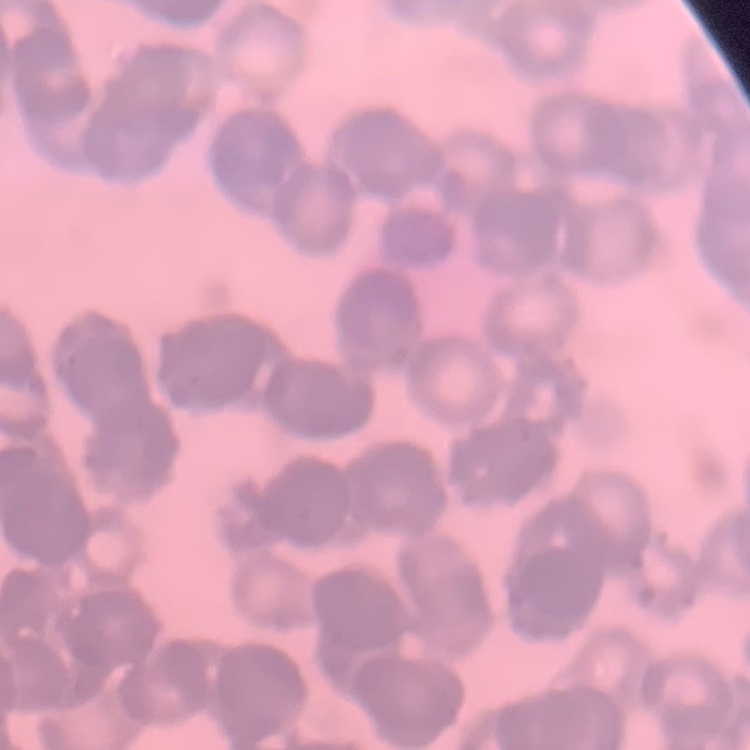
Summary:
  - Erythrocyte morphology: rouleaux formation
  - Preparation: thin blood smear
  - Stain: Field's or Giemsa
  - Image type: square crop of a larger photomicrograph